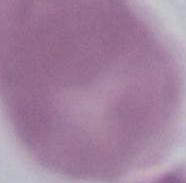
Summary:
  - Modality: micrograph
  - Identification: erythrocyte
  - Magnification: 1000x